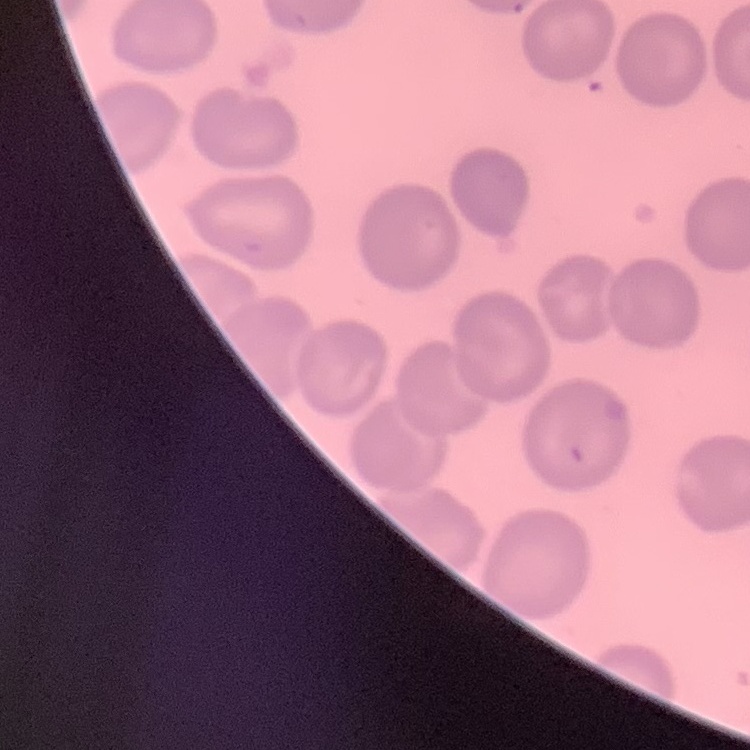

Summary:
  - Erythrocyte morphology: no rouleaux formation
  - Stain: Field's or Giemsa
  - Preparation: thin peripheral smear
  - Image type: square crop of a larger photomicrograph